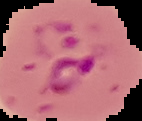
preparation: thin blood film
malaria_status: parasitized
image_type: segmented cell region with the area outside set to black
image_size: 142×121 pixels